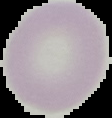
malaria status = uninfected
preparation = thin blood film
image type = segmented cell region on a black background
image size = 112×118 pixels